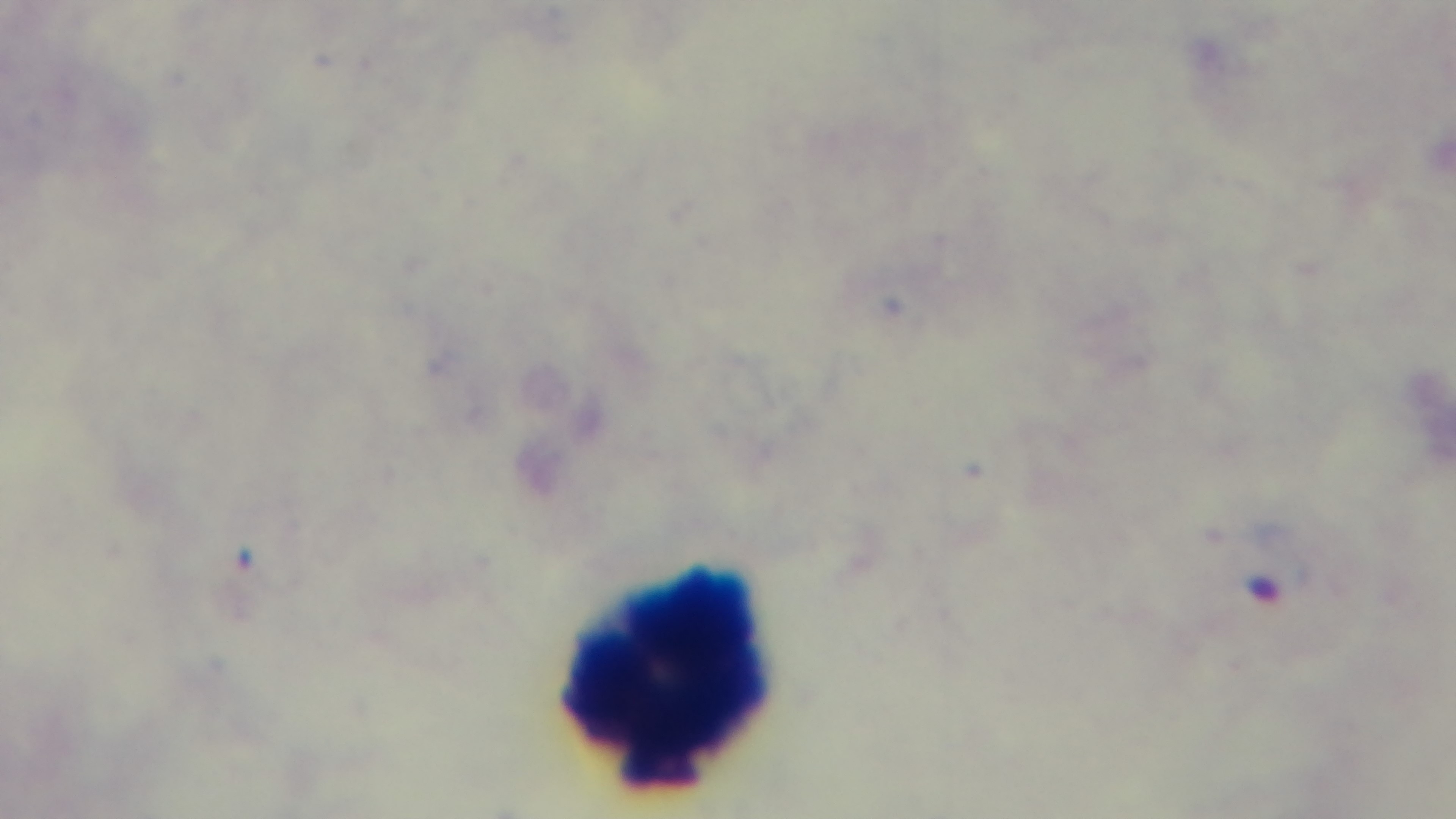
Malaria status: infected. Giemsa stain. Photomicrograph. One field from the slide. Oil-immersion objective, 100x. Captured with a mounted 4K digital camera. Preparation: thick.